Locate every Plasmodium parasite and every leukocyte.
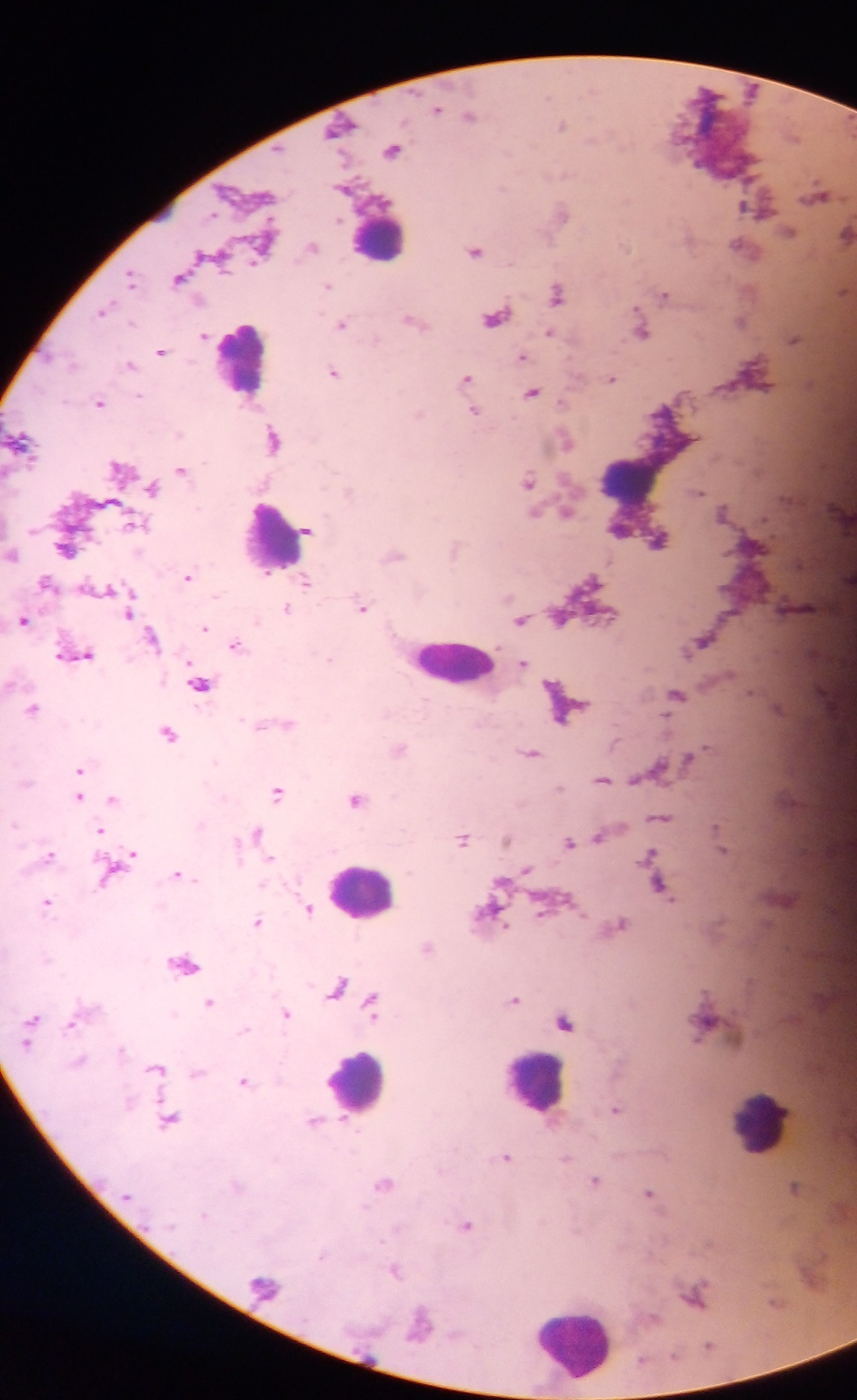
Approximate centers as (x, y) in pixels.
Plasmodium parasites: (437, 108), (470, 116), (561, 126), (391, 150), (818, 194), (753, 208), (562, 212), (791, 232), (847, 234), (313, 247), (740, 247), (475, 251), (131, 276), (179, 278), (328, 286), (558, 295), (665, 296), (104, 311), (411, 319), (742, 321), (341, 324), (492, 327), (549, 333), (643, 333), (204, 336), (794, 339), (161, 351), (522, 357), (72, 364), (129, 364), (334, 372), (466, 379), (612, 379), (531, 393), (99, 402), (475, 411), (18, 439), (273, 439), (566, 442), (181, 470), (528, 481), (152, 488), (698, 491), (349, 492), (566, 512), (723, 513), (133, 523), (306, 531), (659, 540), (64, 550), (188, 576), (44, 583), (590, 583), (306, 584), (362, 607), (287, 609), (129, 613), (561, 618), (24, 620), (521, 620), (205, 628), (153, 638), (235, 645), (81, 655), (331, 659), (524, 663), (199, 684), (677, 695), (33, 708), (568, 711), (288, 724), (169, 733), (399, 749), (531, 753), (79, 769), (638, 777), (603, 780), (559, 788), (277, 792), (78, 797), (112, 798), (356, 800), (661, 817), (101, 831), (255, 833), (600, 837), (463, 838), (507, 840), (569, 843), (723, 849), (132, 854), (49, 855), (650, 856), (270, 860), (527, 869), (111, 873), (178, 875), (661, 886), (560, 902), (47, 903), (310, 909), (543, 909), (257, 922), (619, 925), (428, 948), (184, 963), (337, 987), (514, 999), (209, 1002), (372, 1005), (286, 1014), (32, 1019), (565, 1022), (70, 1024), (26, 1044), (120, 1049), (79, 1061), (156, 1069), (198, 1074), (244, 1081), (616, 1109), (169, 1121), (314, 1121), (506, 1157), (567, 1159), (595, 1180), (384, 1184), (795, 1186), (649, 1193), (467, 1225), (322, 1255), (395, 1270).
Leukocytes: (379, 237), (241, 358), (633, 479), (270, 538), (454, 662), (362, 889), (535, 1082), (357, 1083), (762, 1122), (573, 1340).

Summary:
  - Preparation: thick blood film
  - Image size: 857×1400 pixels
  - Capture: mobile-phone photograph through a microscope
  - Field of view: single
  - Country: Ghana